Describe the morphology of the red blood cells.
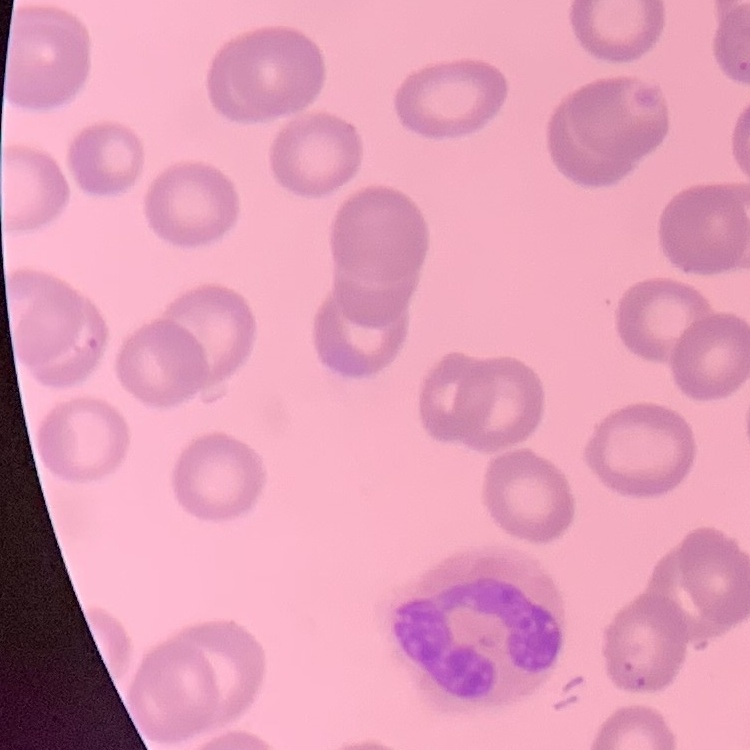

They show no rouleaux formation.

Summary:
  - Preparation: thin blood smear
  - Stain: Field's or Giemsa
  - Image type: square crop of a larger photomicrograph